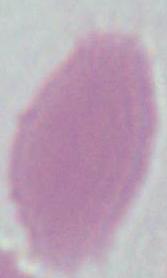
1000x magnification. A red blood cell is seen. Micrograph.